Outline platelets.
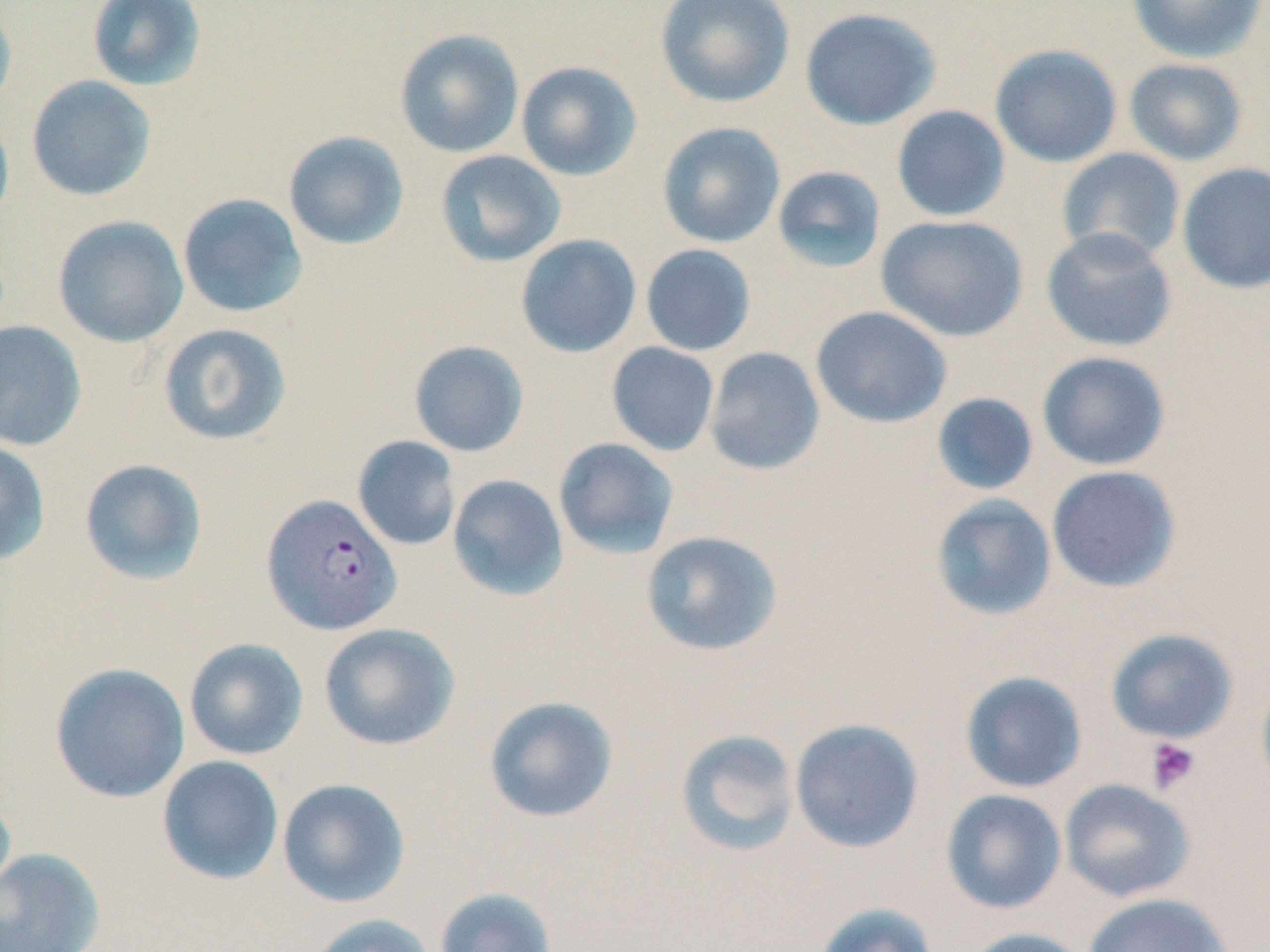
Approximate bounding boxes as [x1, y1, x2, y2] in pixels.
Platelets: [1145, 736, 1201, 795].

Summary:
  - Plasmodium falciparum-infected red blood cell locations: [261, 494, 402, 636]
  - Uninfected red blood cell locations: [86, 0, 207, 92], [655, 0, 796, 108], [1127, 0, 1267, 63], [0, 3, 17, 116], [799, 7, 941, 130], [394, 28, 524, 158], [990, 44, 1122, 168], [1123, 57, 1248, 166], [516, 61, 642, 181], [26, 75, 157, 202], [891, 105, 1010, 222], [0, 110, 15, 231], [656, 122, 785, 249], [283, 131, 410, 251], [1056, 148, 1185, 265], [435, 150, 567, 267], [1176, 162, 1270, 294], [771, 165, 887, 274], [177, 193, 308, 318], [875, 214, 1029, 342], [52, 215, 189, 348], [1041, 227, 1177, 352], [515, 234, 642, 358], [640, 244, 756, 356], [811, 306, 952, 428], [0, 320, 87, 452], [158, 322, 292, 446], [408, 340, 529, 457], [606, 342, 720, 456], [704, 346, 825, 475], [1037, 351, 1170, 471], [931, 392, 1039, 496], [353, 435, 461, 551], [553, 437, 679, 559], [0, 439, 51, 566], [78, 458, 209, 586], [1046, 465, 1182, 593], [447, 474, 569, 601], [930, 494, 1057, 621], [641, 530, 783, 657], [318, 623, 460, 751], [1104, 627, 1238, 744], [184, 638, 308, 760], [49, 662, 190, 803], [959, 671, 1088, 793], [1256, 673, 1270, 797], [483, 695, 618, 824], [789, 718, 924, 853], [675, 728, 800, 857], [157, 755, 284, 885], [277, 778, 411, 908], [1059, 778, 1196, 902], [0, 787, 16, 904], [941, 789, 1067, 914], [0, 848, 105, 952], [434, 886, 558, 952], [1082, 892, 1234, 952], [813, 902, 939, 952], [305, 913, 437, 952], [961, 927, 1092, 952]
  - Slide-level diagnosis: Plasmodium falciparum
  - Modality: optical microscopy
  - Image size: 1270×952 pixels
  - Magnification: 1000x
  - Stain: May-Grünwald-Giemsa
  - Field of view: single
  - Preparation: thin blood smear